Locate and identify every blood parasite.
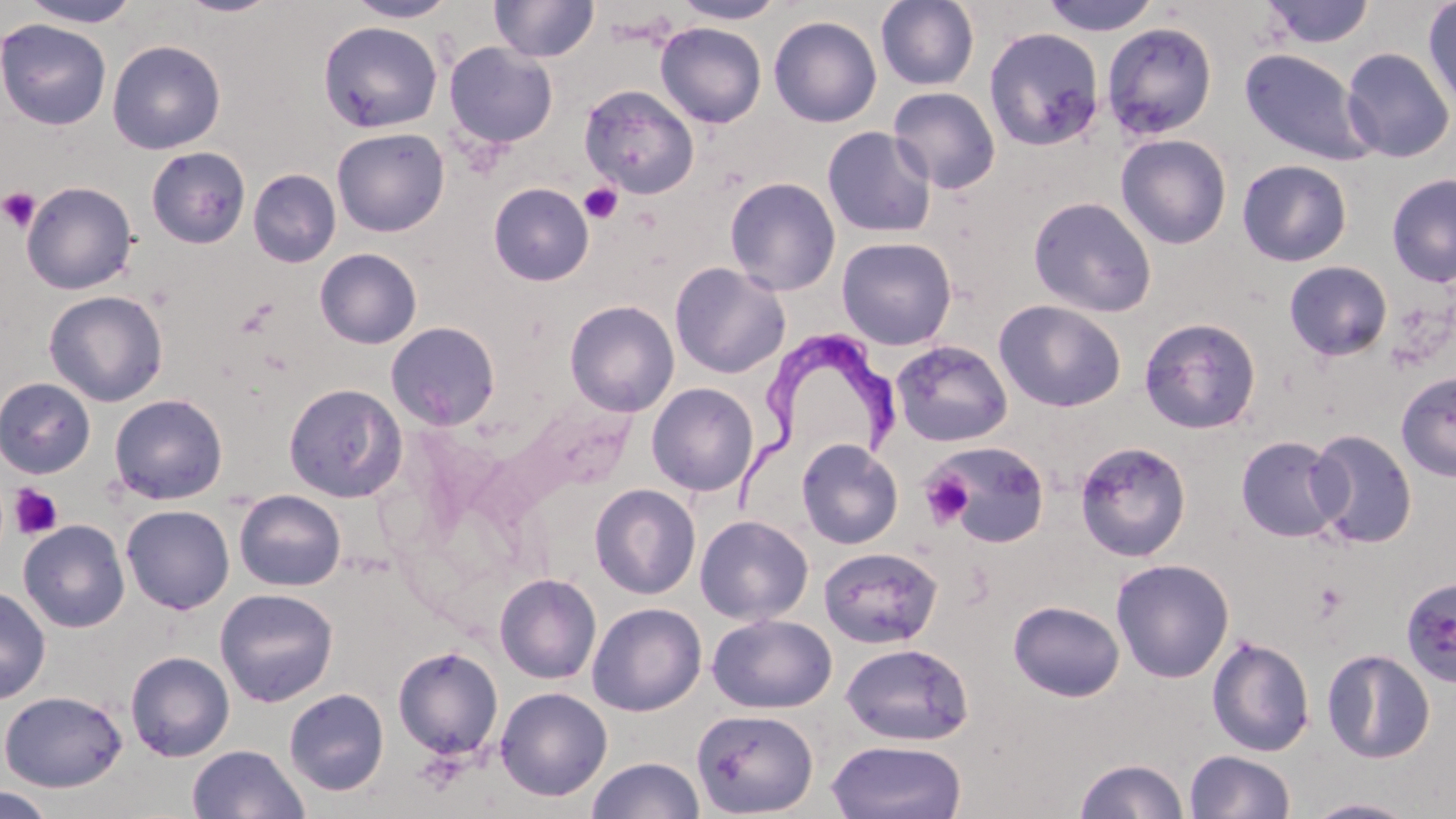

Approximate bounding boxes as (x1, y1, x2, y2) in pixels.
Trypanosoma brucei: (725, 330, 908, 530).
No Plasmodium falciparum, Plasmodium ovale, Plasmodium malariae, Plasmodium vivax, or Babesia divergens observed.

Summary:
  - Platelet locations: (579, 182, 623, 224), (0, 186, 42, 233), (919, 470, 974, 530), (9, 485, 64, 540), (1313, 580, 1348, 620)
  - Uninfected red blood cell locations: (174, 0, 282, 18), (344, 0, 458, 23), (490, 0, 599, 63), (672, 0, 786, 25), (875, 0, 980, 91), (1039, 0, 1163, 36), (19, 1, 141, 28), (1261, 1, 1375, 49), (1422, 2, 1456, 115), (768, 15, 882, 127), (0, 18, 113, 131), (318, 20, 443, 133), (1102, 21, 1218, 140), (655, 22, 767, 128), (984, 27, 1105, 150), (107, 39, 226, 154), (444, 42, 558, 149), (1341, 47, 1455, 163), (1238, 48, 1376, 166), (579, 84, 699, 198), (888, 86, 1001, 195), (822, 126, 937, 238), (331, 127, 450, 237), (1116, 134, 1232, 249), (145, 146, 251, 249), (1236, 159, 1353, 267), (248, 169, 341, 268), (1387, 173, 1456, 287), (724, 177, 841, 296), (21, 181, 138, 294), (488, 182, 594, 286), (1028, 196, 1157, 317), (836, 236, 957, 350), (314, 248, 422, 349), (1284, 260, 1393, 361), (669, 262, 791, 379), (44, 290, 168, 406), (564, 299, 680, 417), (993, 299, 1126, 412), (1138, 317, 1262, 435), (386, 321, 501, 430), (890, 340, 1013, 447), (1396, 370, 1456, 482), (0, 377, 96, 479), (284, 382, 406, 503), (647, 382, 759, 496), (108, 393, 228, 505), (1308, 429, 1417, 549), (1235, 435, 1346, 542), (797, 439, 903, 549), (1075, 440, 1192, 561), (928, 441, 1050, 548), (589, 483, 701, 600), (233, 489, 346, 591), (121, 504, 235, 614), (695, 515, 813, 625), (18, 520, 130, 633), (818, 545, 943, 649), (1110, 558, 1234, 683), (494, 573, 602, 684), (1400, 575, 1456, 688), (0, 585, 51, 705), (214, 588, 339, 707), (1008, 600, 1125, 702), (587, 602, 707, 716), (707, 613, 837, 714), (1206, 635, 1315, 757), (840, 642, 974, 746), (392, 646, 504, 760), (1322, 649, 1436, 763), (125, 651, 235, 762), (495, 686, 613, 801), (284, 688, 389, 796), (0, 690, 128, 792), (691, 708, 819, 818), (826, 740, 967, 819), (187, 744, 310, 819), (1184, 750, 1296, 819), (587, 756, 704, 818), (1074, 759, 1189, 818), (0, 787, 56, 819), (1304, 797, 1421, 818)
  - Slide-level diagnosis: Trypanosoma brucei
  - Stain: May-Grünwald-Giemsa
  - Magnification: 1000x
  - Modality: optical microscopy
  - Field of view: one of a larger specimen
  - Image size: 1456×819 pixels
  - Preparation: thin blood film